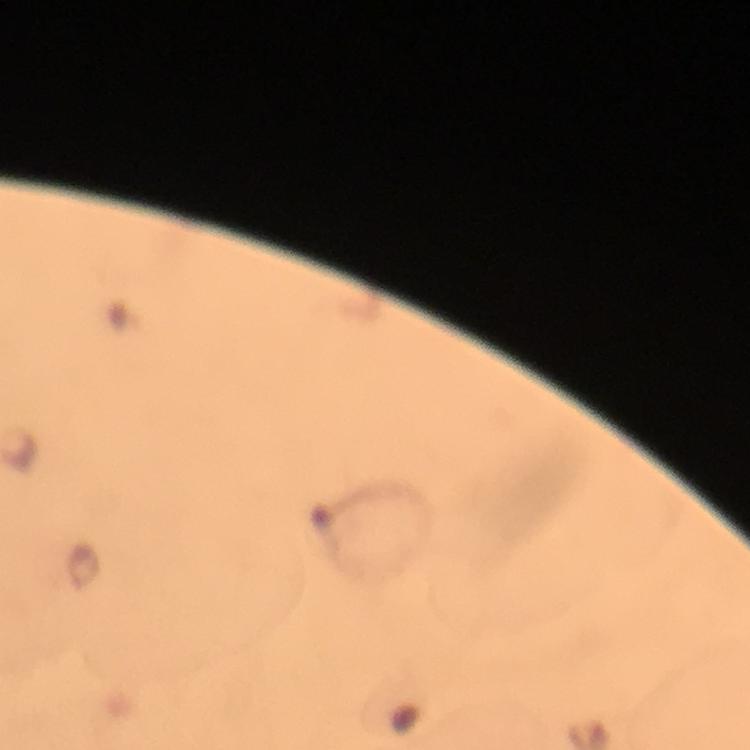
Approximate centers as [x, y] in pixels.
Summary:
  - Plasmodium parasite locations: [81, 565]
  - Image size: 750×750 pixels
  - Stain: Giemsa
  - Immersion oil: used
  - Cropped from: one field of view
  - Magnification: 100x
  - Preparation: thick blood film
  - Capture: smartphone photograph through a microscope
  - Context: from a diagnostic examination for malaria